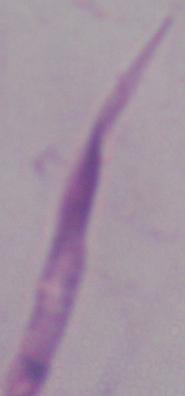

A Leishmania parasite is seen. Photomicrograph. 1000x magnification.